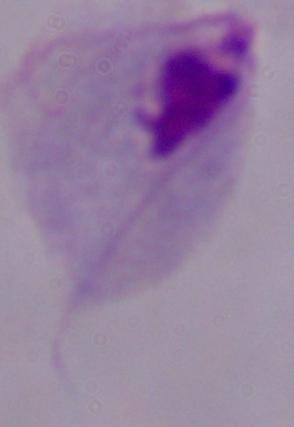

Summary:
  - Magnification: 1000x
  - Identification: trichomonad
  - Modality: photomicrograph